Give the position of every malaria parasite and every leukocyte.
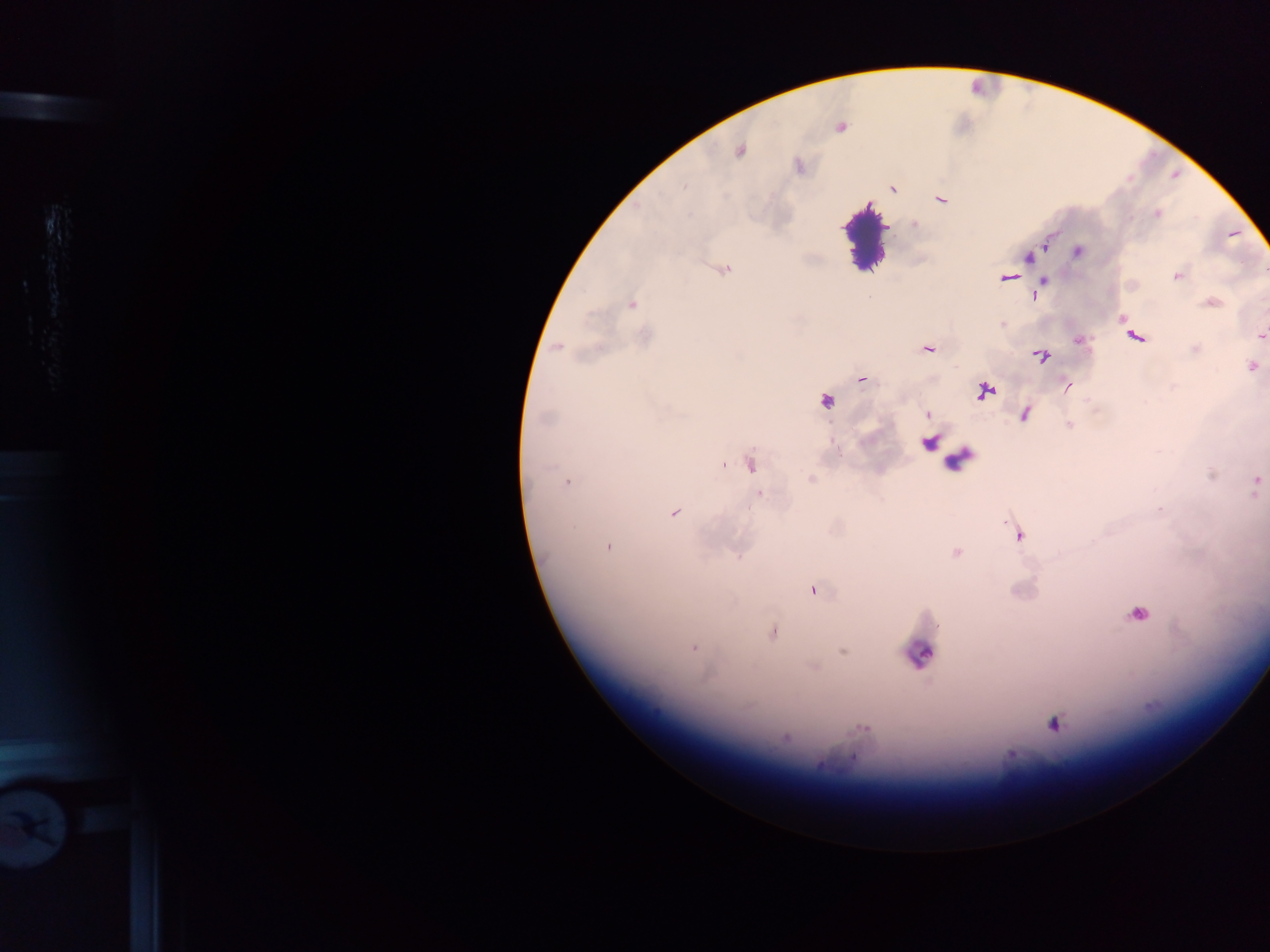

Approximate centers as x y in pixels.
Malaria parasites: 839 128; 740 150; 892 189; 941 199; 1156 213; 914 225; 1044 242; 1077 251; 1028 257; 723 269; 1177 275; 1007 277; 1044 281; 1041 287; 1035 296; 1211 302; 631 304; 1123 319; 1003 323; 1261 335; 1135 336; 645 338; 1079 341; 557 346; 927 348; 1195 349; 1040 356; 1251 366; 861 378; 1067 386; 983 391; 825 400; 927 414; 1023 414; 1069 424; 929 442; 751 463; 723 464; 811 480; 566 481; 1255 483; 760 495; 673 512; 1019 534; 608 546; 956 552; 814 590; 1138 613; 772 632; 692 647; 843 652; 812 666; 1053 723; 863 727; 785 738; 1011 755.
Leukocytes: 865 232; 957 459; 918 654.

Summary:
  - Field of view: single
  - Image size: 1270×952 pixels
  - Country: Ghana
  - Preparation: thick blood film
  - Capture: mobile-phone photograph through a microscope